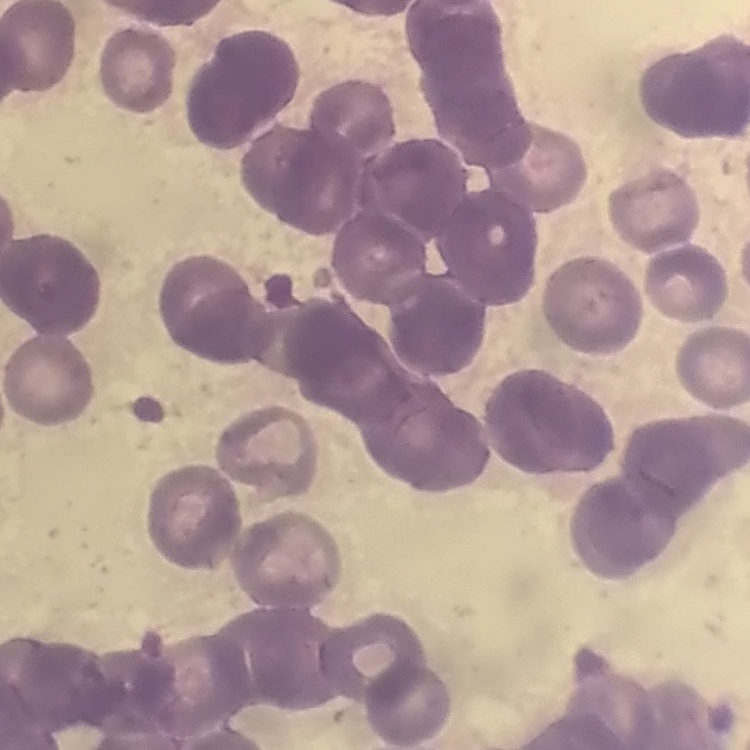

The erythrocytes exhibit rouleaux formation. Stained with either Field's or Giemsa. Square crop of a larger photomicrograph. Thin peripheral smear.